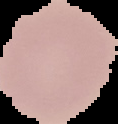
{
  "malaria_status": "uninfected",
  "preparation": "thin blood film",
  "image_size": "118×124 pixels",
  "image_type": "segmented cell region on a black background"
}